Assess for Plasmodium parasites.
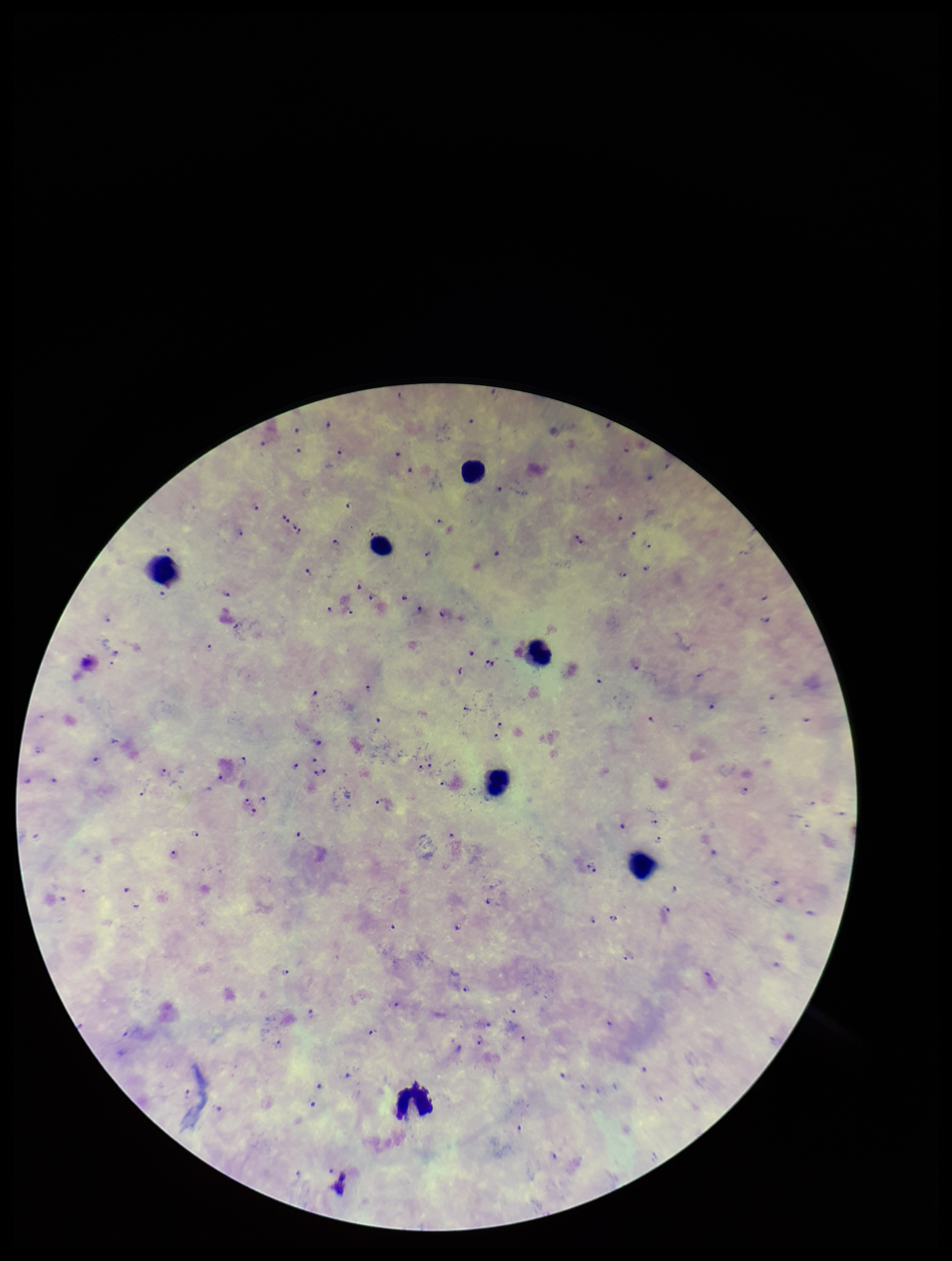
Detected.

Giemsa stain. Preparation: thick. Parasite count: 97. Image is 952×1261 pixels. Photographed through the microscope eyepiece with a smartphone camera. Patient malaria status: positive. Leukocyte count: 7. Single field of view. Species reported for this patient: Plasmodium falciparum.